Comment on the morphology of the red blood cells.
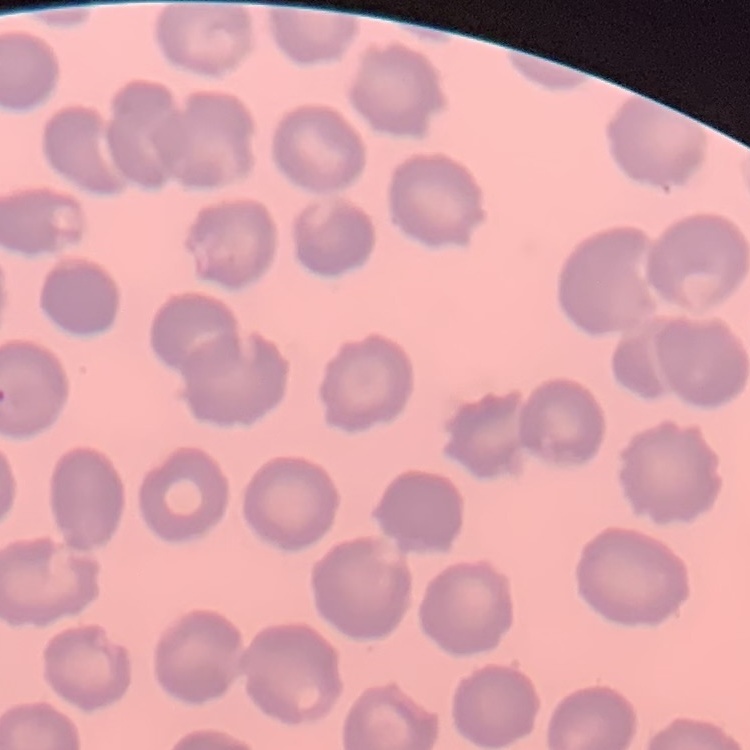

They show no rouleaux formation.

{
  "preparation": "thin blood smear",
  "image_type": "square crop of a larger photomicrograph",
  "stain": "Field's or Giemsa"
}